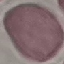 Malaria status: uninfected. Cell patch, automatically extracted from a larger field of view and resized to 64 × 64 pixels. Giemsa stain. Thin blood film. Photographed with a smartphone camera at the microscope eyepiece.